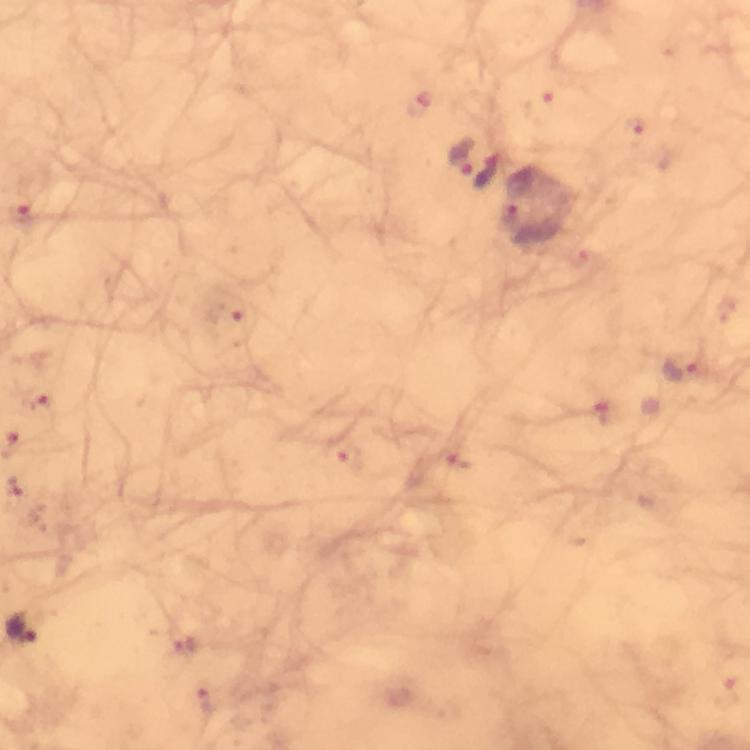

Approximate centers as [x, y] in pixels.
Summary:
  - Plasmodium parasite locations: [541, 109], [635, 134], [461, 155], [486, 170], [22, 217], [513, 218], [225, 319], [686, 367], [38, 401], [606, 413], [351, 459], [457, 460], [25, 631], [204, 701]
  - Capture: smartphone camera through the microscope
  - Preparation: thick blood smear
  - Immersion oil: applied
  - Context: from a diagnostic examination for malaria
  - Image size: 750×750 pixels
  - Cropped from: a single field of view
  - Magnification: 100x
  - Stain: Giemsa